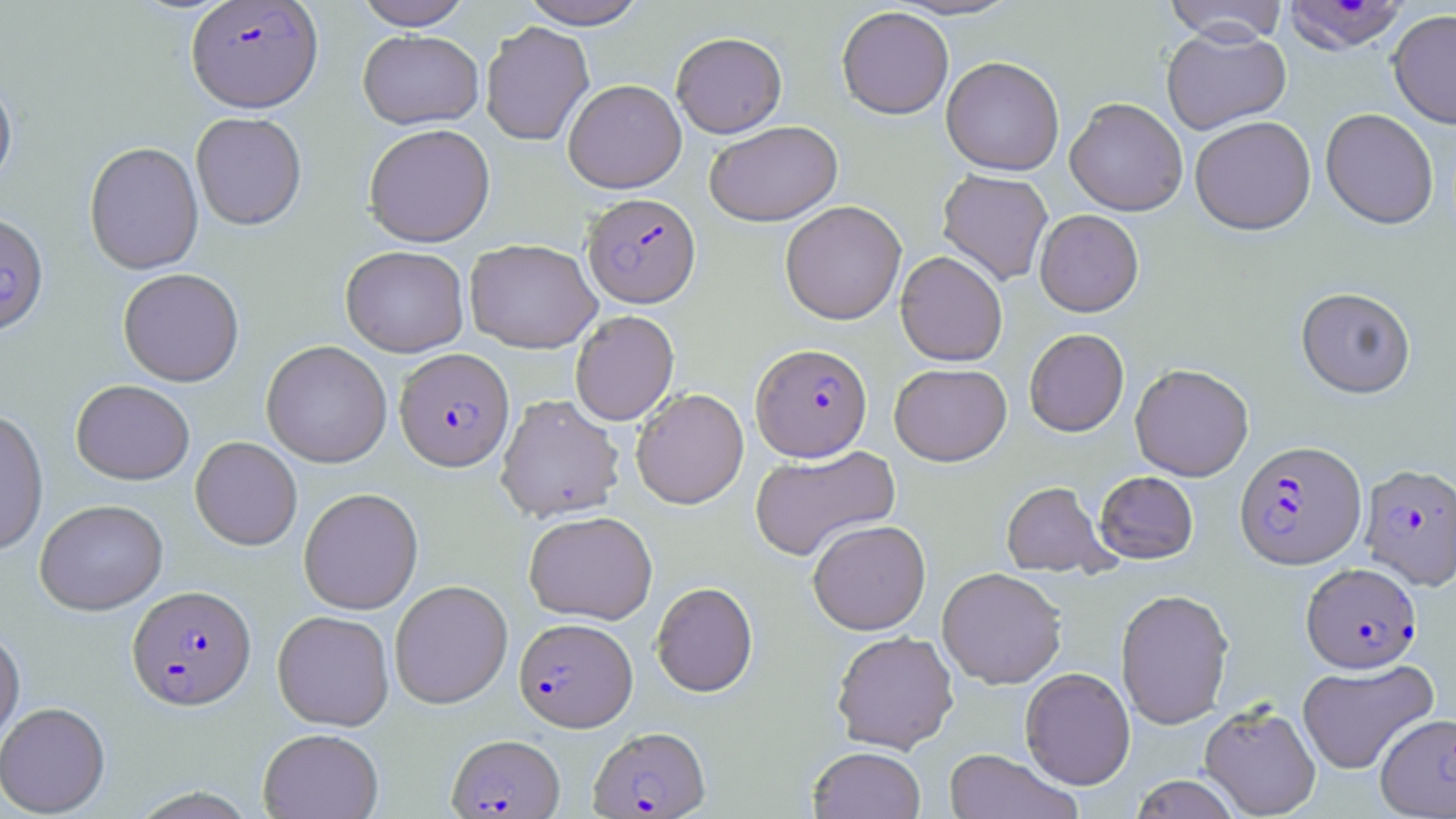
Approximate bounding boxes as (x1,y1)-(x2,y2) corner pairs in pixels. Plasmodium falciparum-infected red blood cell locations (subset): (185,1)-(323,113), (1281,1)-(1411,54), (582,192)-(701,307), (0,211)-(49,335), (750,343)-(872,461), (394,348)-(514,472), (1234,439)-(1366,570), (1359,463)-(1455,591), (1301,562)-(1421,673), (127,584)-(256,710), (514,617)-(637,731), (588,726)-(710,818), (447,734)-(564,818). Uninfected red blood cell locations (subset): (353,0)-(474,30), (519,0)-(647,29), (885,0)-(1025,21), (1162,0)-(1289,45), (837,6)-(954,119), (1387,9)-(1456,129), (480,21)-(595,146), (1160,26)-(1292,135), (358,30)-(483,129), (671,31)-(787,138), (941,56)-(1065,175), (0,72)-(17,193), (563,79)-(687,193), (1065,97)-(1188,216), (1320,108)-(1438,229), (190,112)-(307,230), (1189,115)-(1316,235), (705,121)-(843,226), (363,123)-(495,247), (84,141)-(204,275), (937,169)-(1053,286), (779,200)-(907,325), (1035,209)-(1144,316), (464,239)-(601,353), (340,245)-(469,357), (895,250)-(1008,366), (117,268)-(244,387), (1296,286)-(1416,398), (569,310)-(679,426), (1024,328)-(1129,436), (261,340)-(392,468), (889,362)-(1011,466), (1130,363)-(1254,481), (71,379)-(195,485), (631,388)-(748,509), (496,394)-(625,522), (0,409)-(49,555), (190,436)-(303,550), (749,444)-(900,562), (1095,471)-(1199,563), (1001,481)-(1115,578), (298,487)-(423,614), (34,499)-(168,615), (524,510)-(658,624), (807,518)-(931,635), (937,567)-(1067,688), (390,580)-(513,708), (651,582)-(757,697), (1115,588)-(1234,729), (272,610)-(394,730), (0,625)-(25,749), (831,630)-(959,754), (1297,658)-(1437,775), (1020,666)-(1136,790), (0,701)-(110,817), (1199,702)-(1322,818), (258,728)-(384,818), (807,746)-(926,818), (943,748)-(1081,819), (1130,774)-(1241,818). Slide-level diagnosis: Plasmodium falciparum. Thin blood film. Optical microscopy. 1000x magnification. May-Grünwald-Giemsa stain. Image is 1456×819 pixels. Single field of view.